Give the preparation type.
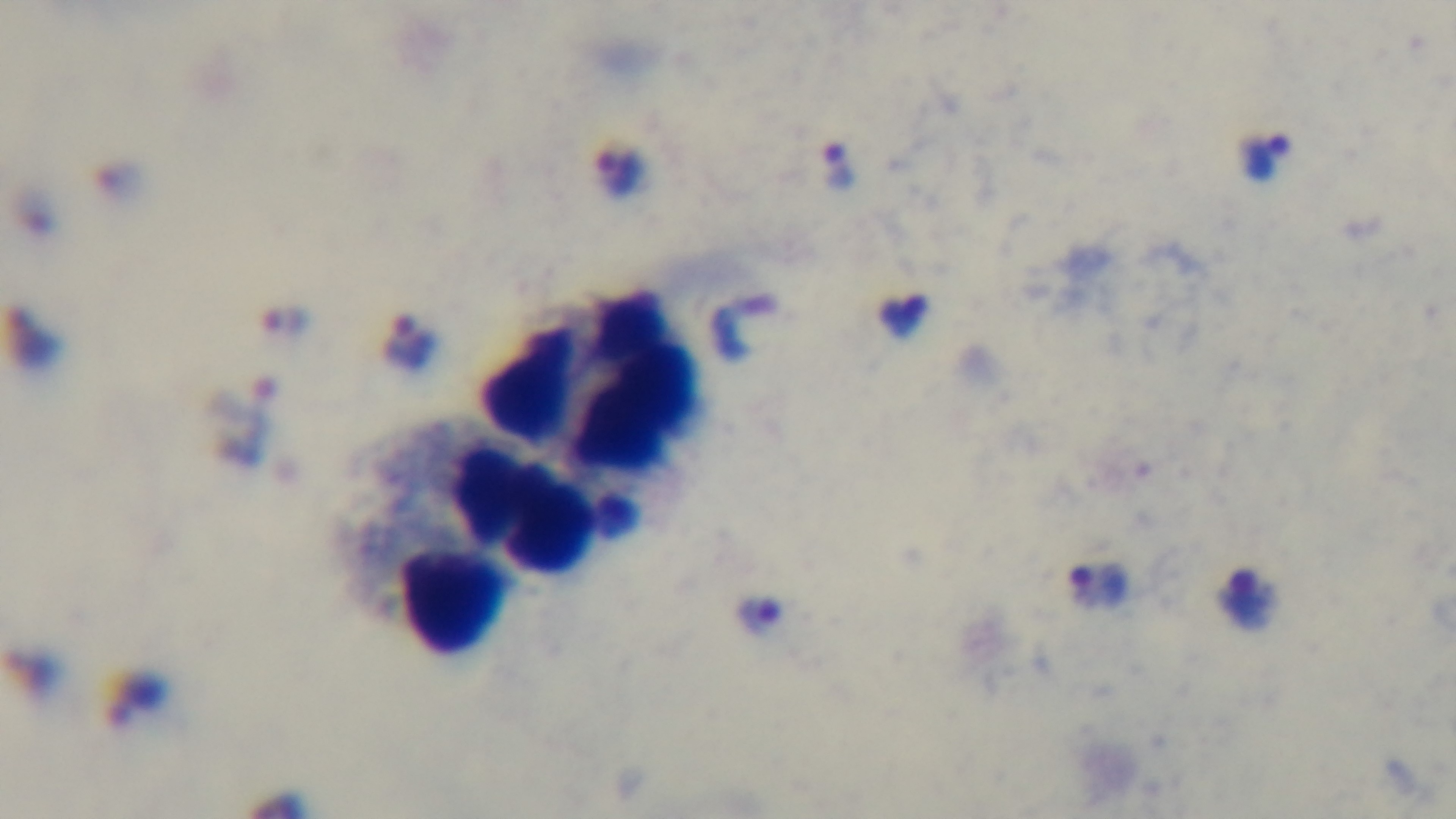
It is a thick blood film.

Captured with a mounted 4K digital camera. Giemsa stain. Malaria status: infected. Photomicrograph. 100x oil-immersion objective. Single field of view.